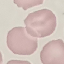 Malaria status: uninfected. Thin blood smear. Giemsa stain. Photographed with a smartphone camera at the microscope eyepiece. Automatically extracted cell patch, resized to 64 × 64 pixels.